Report the malaria status of this cell.
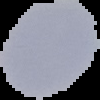

It is uninfected.

preparation = thin blood film
image size = 100×100 pixels
image type = segmented cell region on a black background